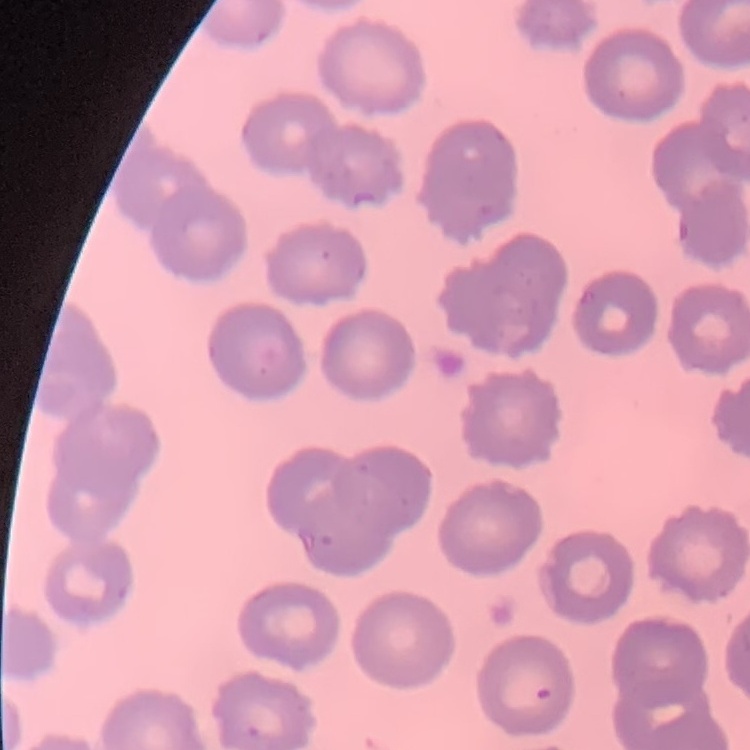

The erythrocytes show no rouleaux formation. Thin blood smear. Stained with either Field's or Giemsa. One tile cut from a larger photomicrograph.